Give the position of every Plasmodium parasite visible.
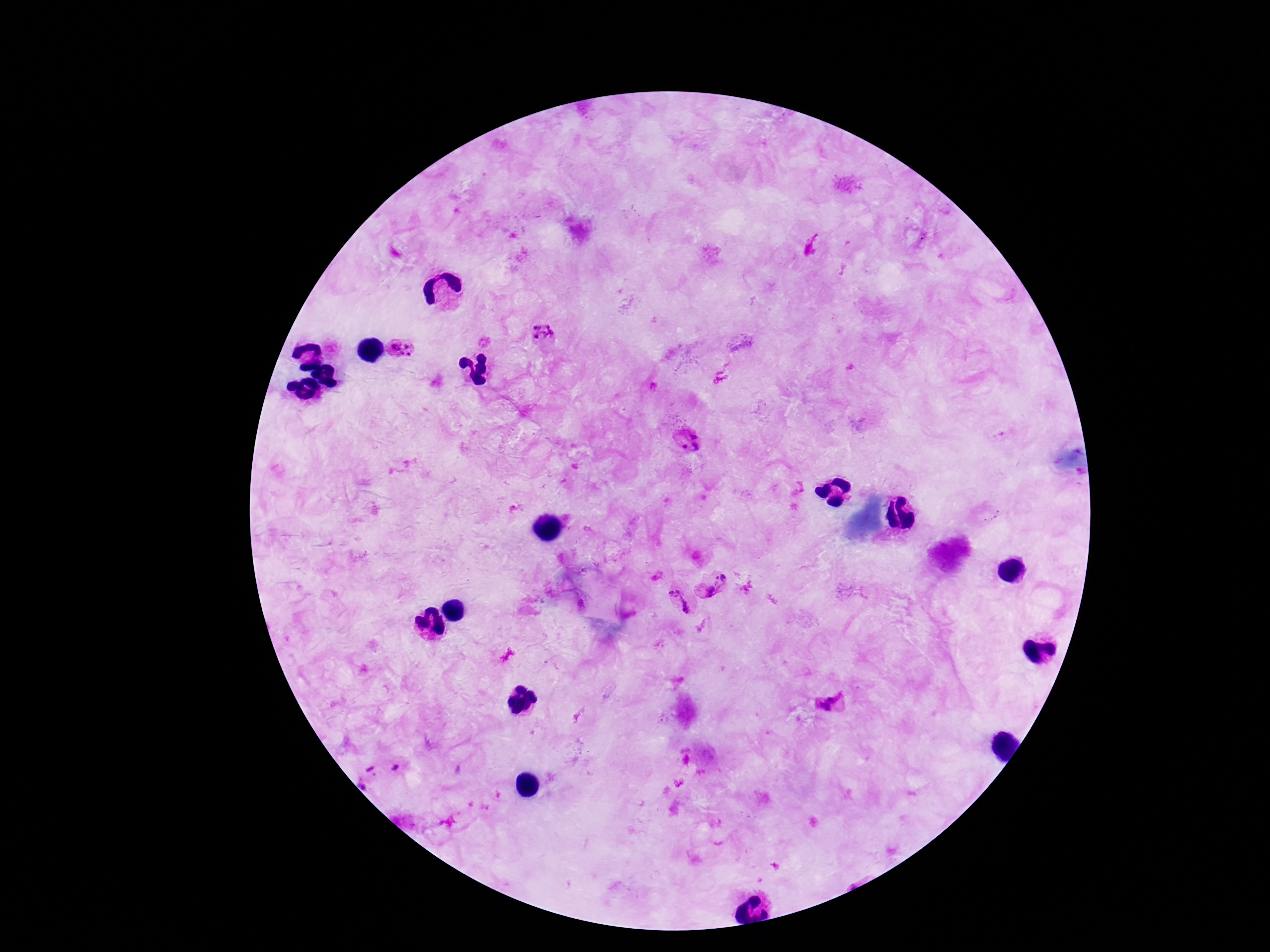

Approximate centers as [x, y] in pixels.
Plasmodium parasites: [543, 331], [402, 349], [690, 444], [723, 578], [707, 591], [675, 600], [830, 704], [395, 767], [372, 770], [363, 785].

Summary:
  - Magnification: 100x
  - Preparation: thick blood smear
  - Field of view: single
  - Patient malaria status: positive
  - Capture: smartphone camera through the microscope eyepiece
  - Stain: Giemsa
  - Image size: 1270×952 pixels